Evaluate for malaria.
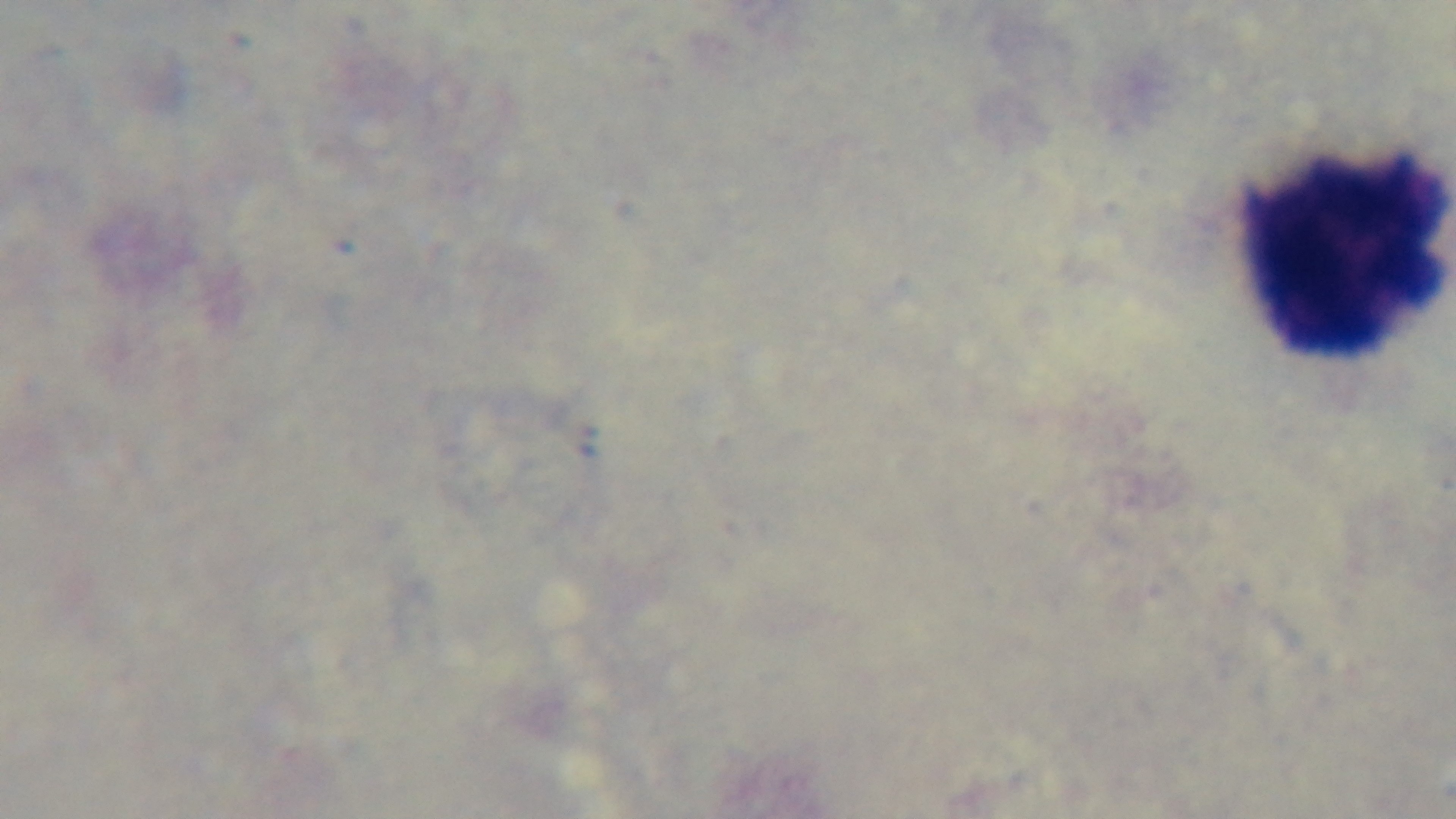

Uninfected.

preparation = thick blood film
stain = Giemsa
capture = mounted 4K digital camera
objective = 100x oil immersion
field of view = one from the slide
modality = light microscopy